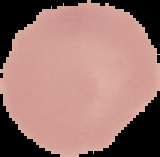
From a thin blood film. Malaria status: uninfected. Image is 160×157 pixels. Segmented cell region on a black background.